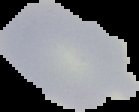

{
  "image_size": "139×112 pixels",
  "preparation": "thin blood film",
  "image_type": "cell region segmented out of the field of view; surrounding area masked to black",
  "malaria_status": "uninfected"
}